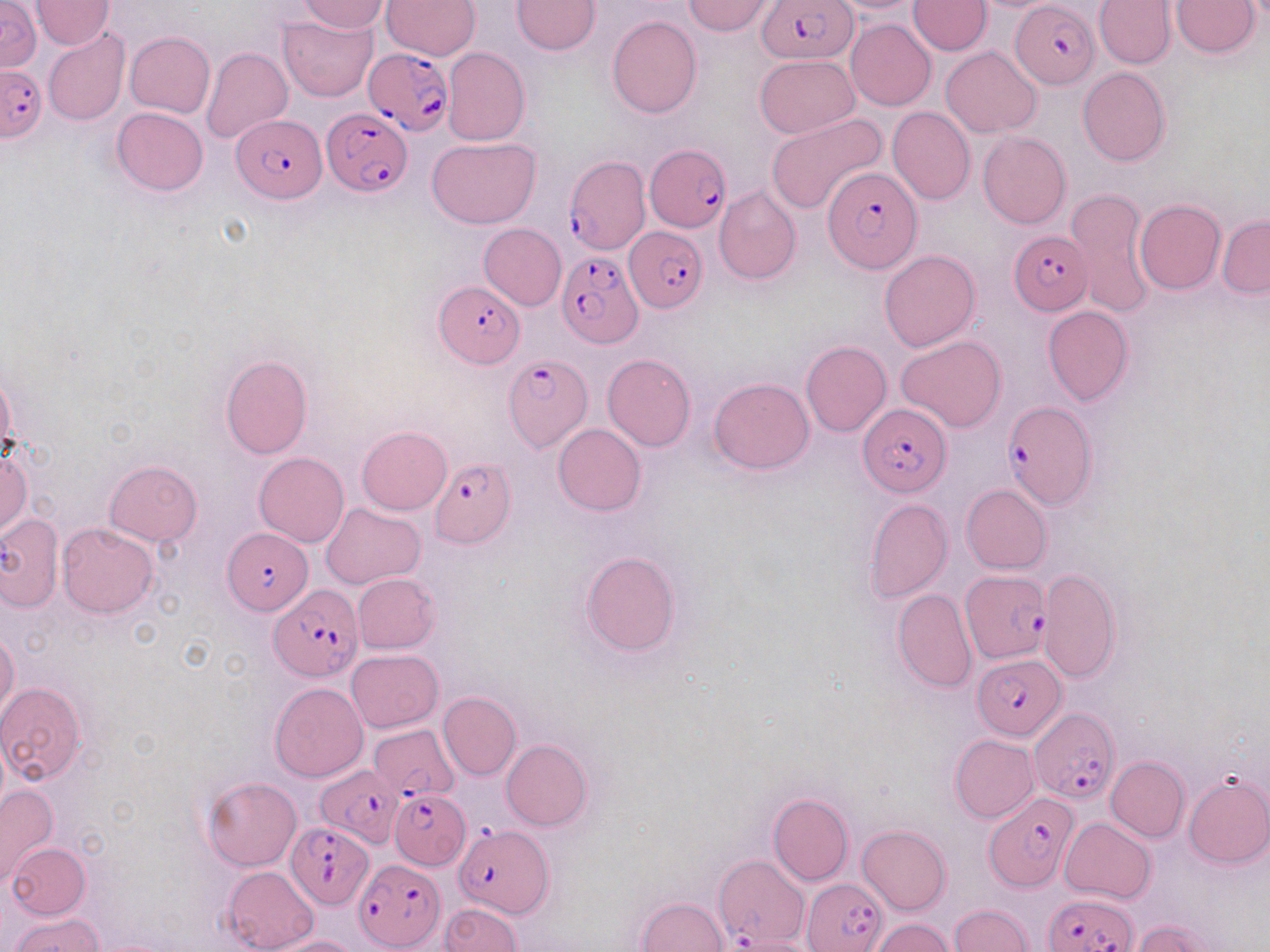
Approximate bounding boxes as (x1,y1)-(x2,y2) corner pairs in pixels. Uninfected red blood cell locations: (30,0)-(114,50), (382,0)-(480,60), (512,0)-(601,55), (683,0)-(776,36), (908,0)-(990,55), (1171,0)-(1259,58), (1,1)-(41,72), (298,1)-(389,33), (827,1)-(927,15), (1093,1)-(1175,69), (278,15)-(376,101), (607,15)-(701,119), (846,18)-(936,110), (42,29)-(129,126), (124,31)-(216,119), (442,47)-(529,147), (941,47)-(1042,136), (202,48)-(292,146), (755,54)-(860,137), (1078,67)-(1170,166), (112,107)-(208,196), (887,107)-(976,204), (766,114)-(888,216), (978,131)-(1071,229), (427,137)-(540,228), (714,185)-(801,284), (1068,189)-(1153,317), (1135,199)-(1226,294), (1217,215)-(1269,297), (478,223)-(567,310), (878,249)-(981,351), (1043,305)-(1134,404), (896,335)-(1007,432), (800,341)-(892,437), (602,353)-(695,451), (219,356)-(313,459), (708,377)-(814,473), (553,424)-(646,516), (356,426)-(452,515), (0,446)-(31,538), (254,453)-(350,547), (104,460)-(203,545), (962,484)-(1052,574), (865,498)-(952,603), (322,504)-(425,588), (0,512)-(62,611), (58,524)-(158,617), (581,551)-(681,657), (1037,567)-(1122,684), (352,573)-(441,653), (892,587)-(977,692), (0,630)-(20,720), (346,649)-(443,732), (0,682)-(87,784), (269,682)-(368,782), (438,691)-(521,781), (951,735)-(1039,822), (501,739)-(593,830), (1106,756)-(1189,842), (1183,773)-(1270,868), (202,776)-(302,870), (0,784)-(59,886), (768,793)-(854,885), (1059,817)-(1156,903), (856,825)-(951,915), (7,842)-(91,919), (223,865)-(319,952), (635,897)-(729,952), (440,903)-(521,951), (948,904)-(1034,951), (10,913)-(105,951), (1131,918)-(1223,952), (870,919)-(955,952), (726,935)-(819,952), (264,936)-(361,952). Plasmodium falciparum-infected red blood cell locations: (757,0)-(859,64), (1012,2)-(1099,89), (363,48)-(454,138), (0,66)-(45,140), (321,106)-(409,197), (233,113)-(326,201), (644,144)-(728,229), (563,153)-(650,256), (824,164)-(923,272), (625,228)-(707,314), (1008,230)-(1093,314), (554,247)-(642,349), (434,280)-(525,369), (503,354)-(592,450), (1002,401)-(1098,511), (858,404)-(951,497), (428,457)-(517,548), (223,528)-(312,615), (960,572)-(1049,662), (268,585)-(364,678), (972,654)-(1066,741), (1029,708)-(1117,803), (368,723)-(459,802), (316,765)-(400,864), (389,789)-(471,869), (985,793)-(1079,891), (288,821)-(377,909), (450,823)-(560,924), (714,854)-(809,949), (354,860)-(443,950), (804,878)-(887,951), (1043,892)-(1138,952). Slide-level diagnosis: Plasmodium falciparum. Thin blood smear. One field of a larger specimen. May-Grünwald-Giemsa-stained preparation. Image is 1270×952 pixels. 1000x magnification. Light microscopy.